Classify this cell by malaria status.
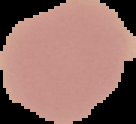

Uninfected.

Image is 136×124 pixels. Segmented cell region on a black background. From a thin blood film.